Report the malaria status of this cell.
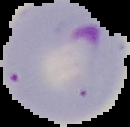
It is parasitized.

Summary:
  - Image type: segmented cell region with the area outside set to black
  - Image size: 130×127 pixels
  - Preparation: thin blood film